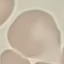

malaria status = uninfected
stain = Giemsa
capture = smartphone camera at the microscope eyepiece
image type = cell patch, automatically extracted from a larger field of view and resized to 64 × 64 pixels
preparation = thin smear